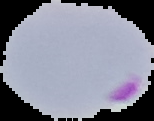 Result: Plasmodium parasites detected. From a thin blood film. Segmented cell region on a black background. Image is 154×121 pixels.